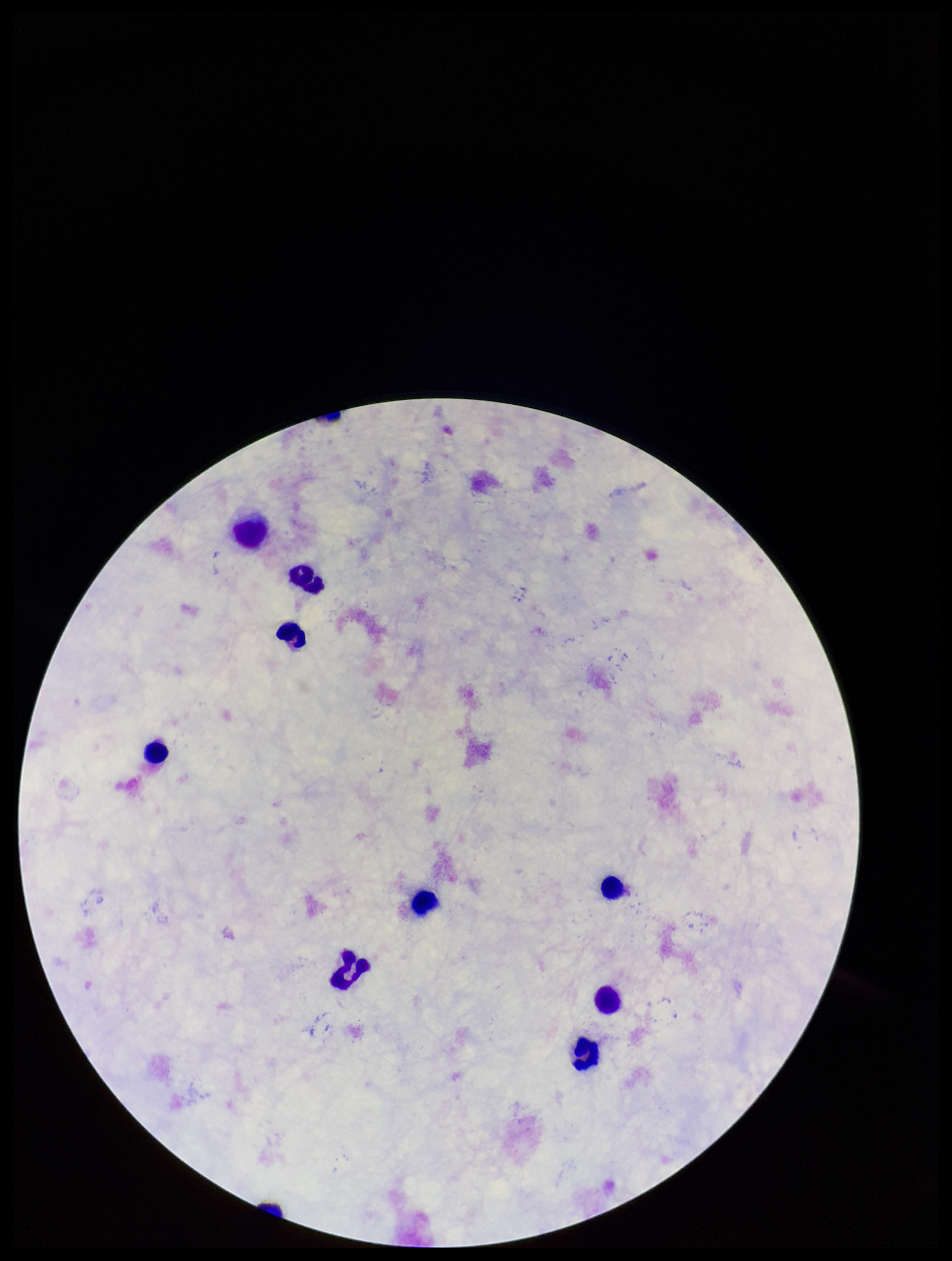
field of view = single
patient malaria status = negative
stain = Giemsa
Plasmodium parasites = none detected
capture = smartphone photograph through the microscope eyepiece
preparation = thick
leukocyte count = 9
parasite count = 0
image size = 952×1261 pixels